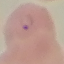
Malaria status: parasitized. Thin smear of blood. Cell patch, automatically extracted from a larger field of view and resized to 64 × 64 pixels. Acquired by smartphone through the microscope eyepiece. Giemsa stain.